Assess the morphology of the erythrocytes.
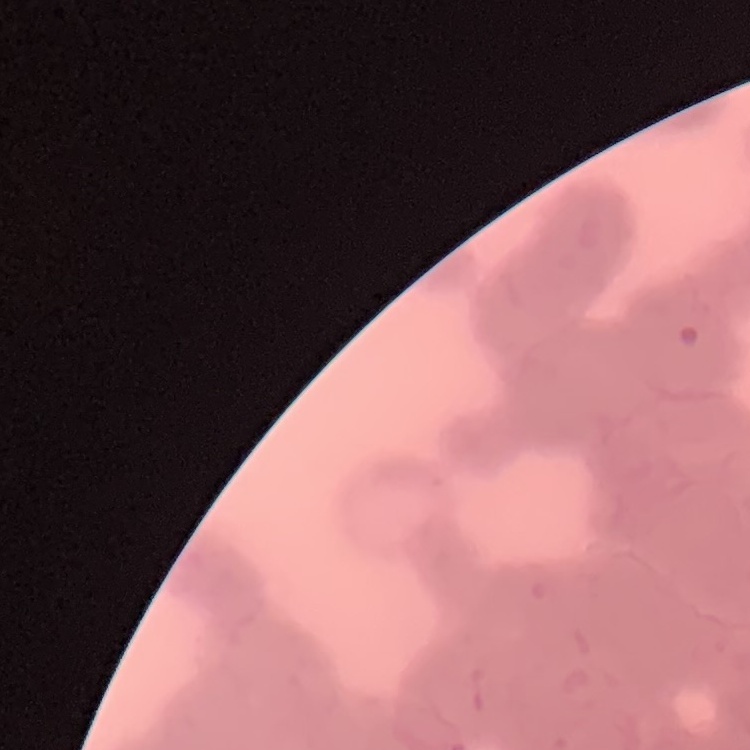
Rouleaux formation.

One tile cut from a larger photomicrograph. Stained with either Field's or Giemsa. Thin blood film.